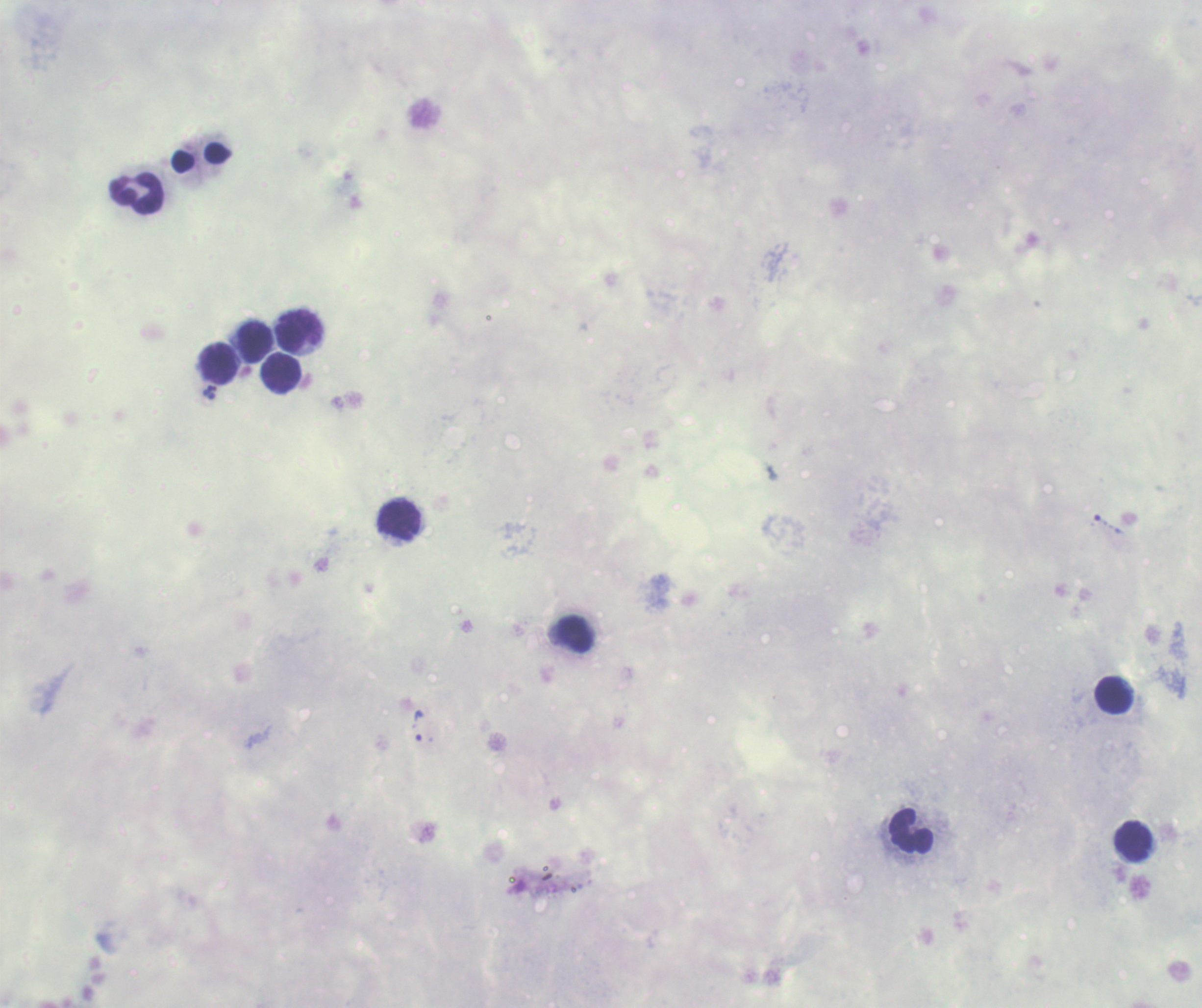

{
  "field_of_view": "one from this slide",
  "magnification": "100x",
  "result": "no Plasmodium parasites detected",
  "image_size": "1202×1008 pixels",
  "leukocyte_locations": "approximate object centers, in pixels from the top-left corner: (x=137, y=193), (x=300, y=331), (x=255, y=342), (x=217, y=363), (x=282, y=372), (x=399, y=521), (x=576, y=633), (x=1114, y=695), (x=912, y=830), (x=1132, y=841)",
  "background_quality": "poor",
  "stain": "Romanowsky",
  "context": "previously used in an actual diagnosis",
  "coloration_quality": "bad",
  "preparation": "thick smear of blood"
}